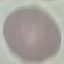 Result: no malaria parasites detected. Thin blood smear. Acquired by smartphone through the microscope eyepiece. Automatically extracted cell patch, resized to 64 × 64 pixels. Giemsa stain.